Classify this cell by malaria status.
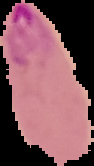

It is parasitized.

{
  "preparation": "thin blood smear",
  "image_size": "94×166 pixels",
  "image_type": "segmented cell region with the area outside set to black"
}